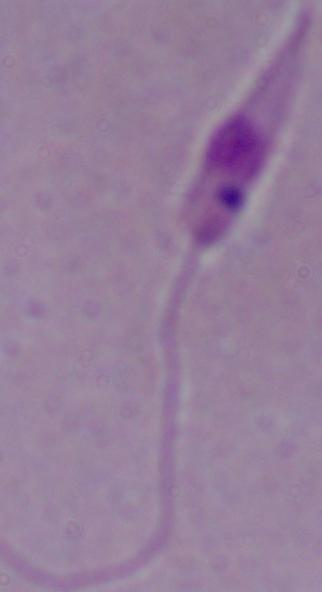
Summary:
  - Modality: micrograph
  - Identification: Leishmania
  - Magnification: 1000x